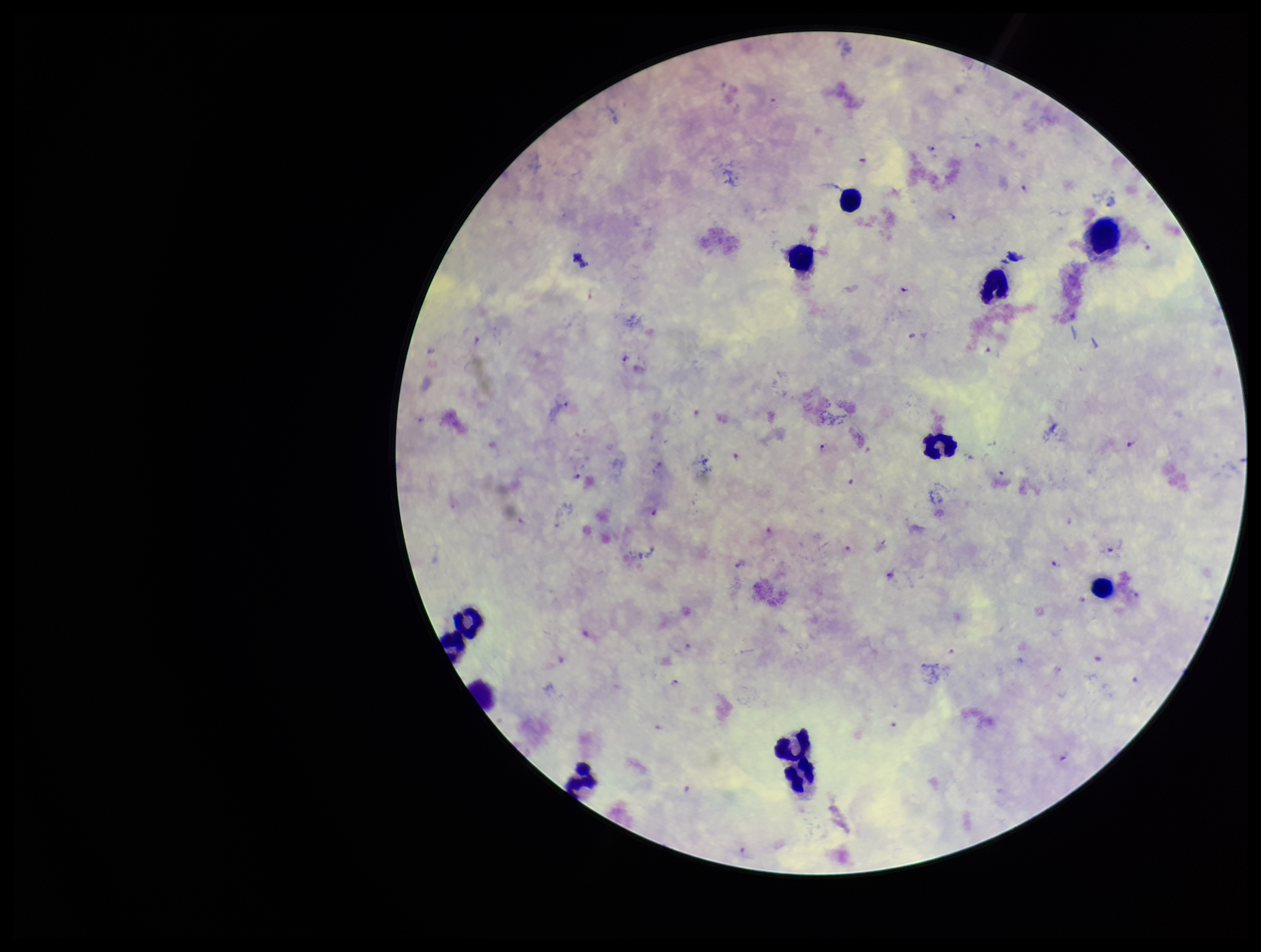
Summary:
  - Capture: smartphone photograph through the microscope eyepiece
  - Preparation: thick smear
  - Leukocyte count: 12
  - Patient malaria status: positive
  - Field of view: one from this slide
  - Stain: Giemsa
  - Parasite count: 36
  - Species reported for this patient: Plasmodium falciparum
  - Plasmodium parasites: detected
  - Image size: 1261×952 pixels